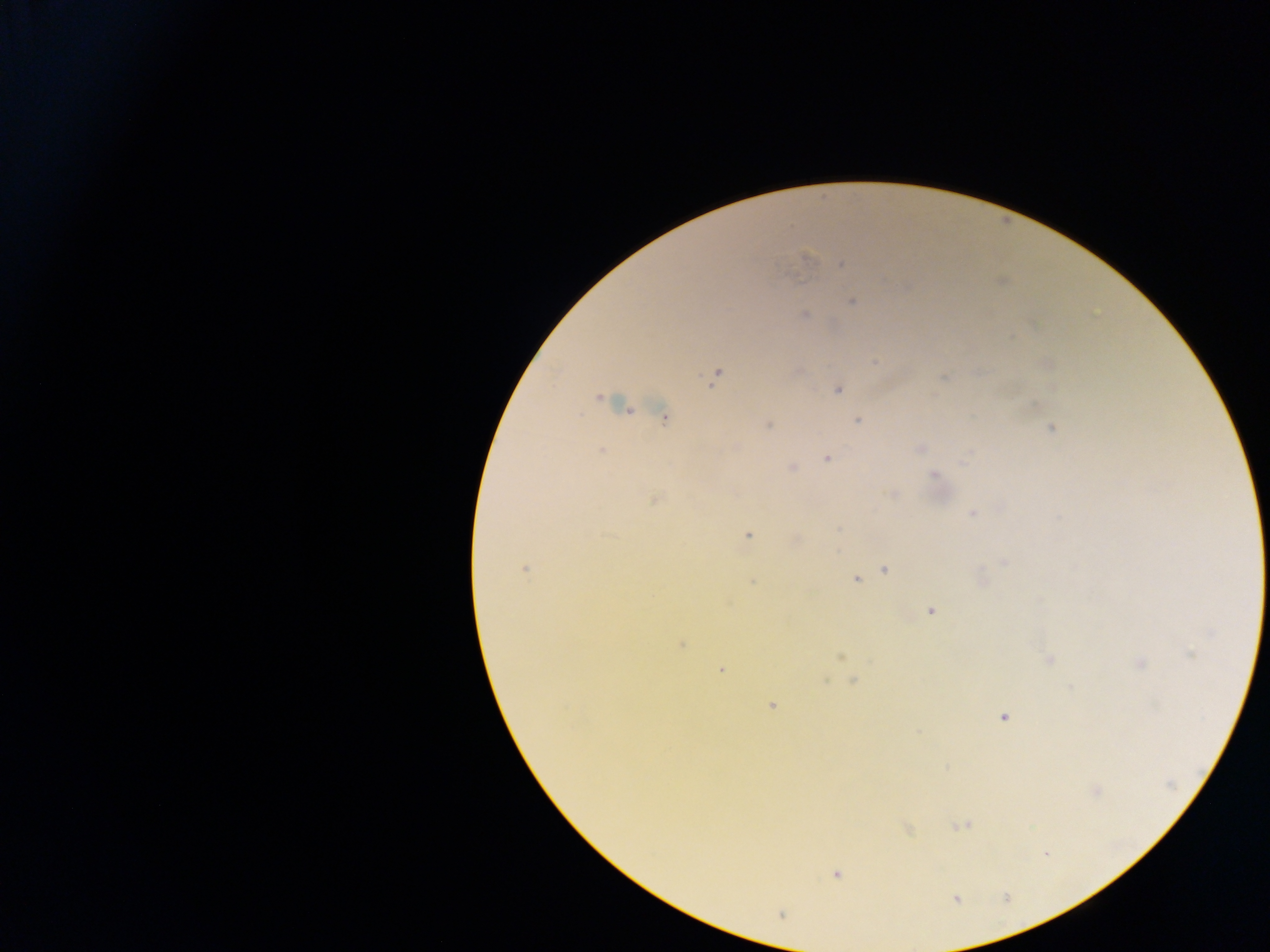

Approximate centers as [x, y] in pixels.
Summary:
  - Malaria parasite locations: [807, 257], [842, 264], [853, 302], [805, 315], [876, 363], [715, 376], [943, 379], [839, 389], [599, 397], [663, 417], [858, 421], [768, 426], [1051, 429], [919, 448], [602, 450], [968, 454], [827, 459], [791, 468], [934, 474], [892, 494], [653, 500], [971, 513], [838, 529], [748, 535], [1003, 563], [524, 569], [885, 570], [856, 580], [753, 582], [931, 611], [1211, 633], [681, 645], [1190, 654], [840, 657], [1049, 660], [1139, 663], [721, 670], [853, 680], [771, 706], [1003, 717], [918, 731], [961, 825], [1045, 854], [836, 874]
  - Preparation: thick blood film
  - Image size: 1270×952 pixels
  - Field of view: single
  - Country: Ghana
  - Capture: mobile-phone photograph through a microscope